Outline each blood parasite and name the species.
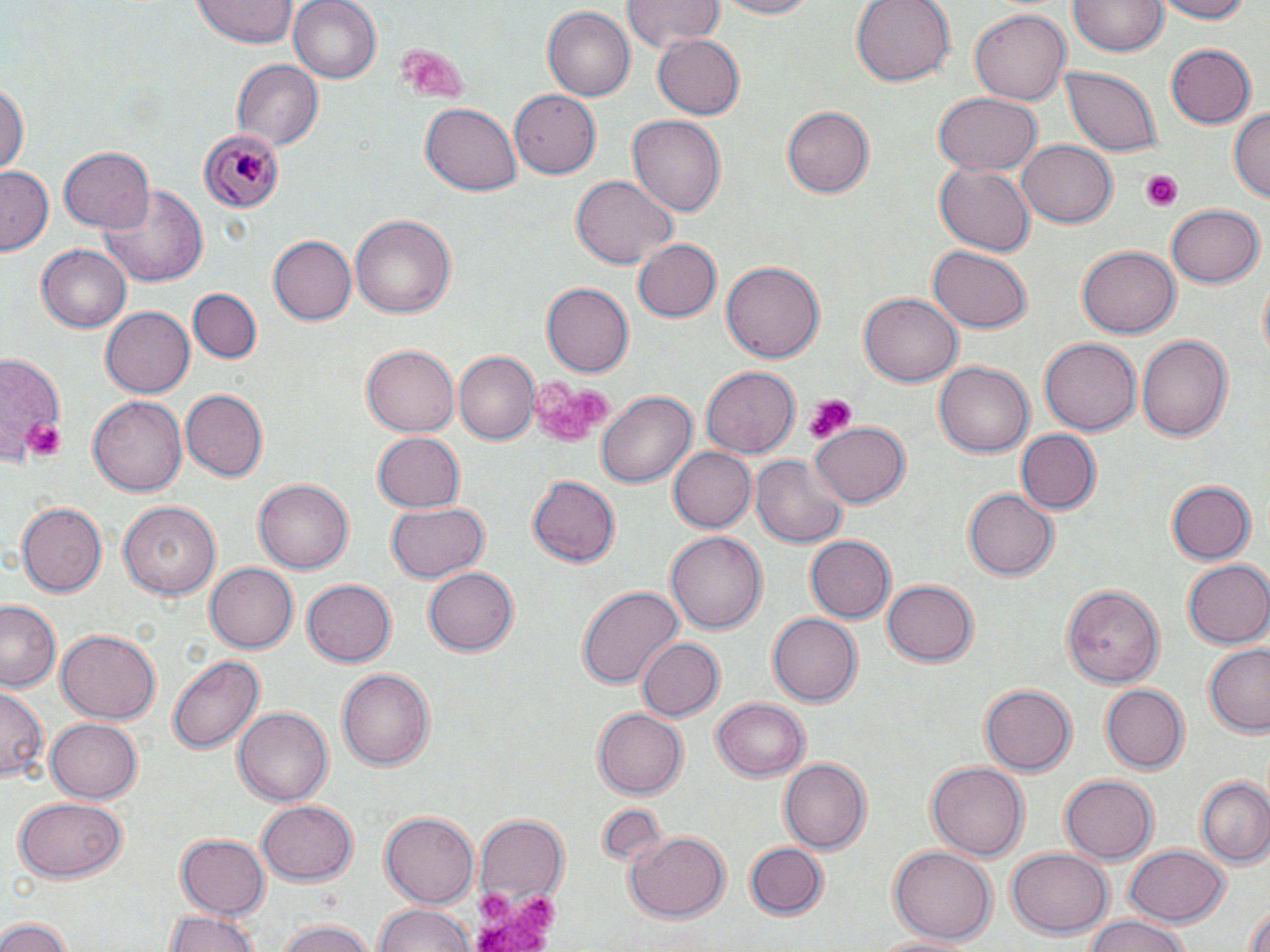

Approximate bounding boxes as (x1,y1)-(x2,y2) corner pairs in pixels.
Plasmodium malariae-infected red blood cells: (199,130)-(286,212).
No Plasmodium falciparum, Plasmodium ovale, Plasmodium vivax, Babesia divergens, or Trypanosoma brucei observed.

slide_level_diagnosis: Plasmodium malariae
field_of_view: one of a larger specimen
preparation: thin blood film
image_size: 1270×952 pixels
uninfected_red_blood_cell_locations: 'approximate bounding boxes as (x1,y1)-(x2,y2) corner pairs in pixels: (195,0)-(298,46), (289,0)-(384,84), (621,0)-(723,53), (704,0)-(820,18), (851,0)-(955,86), (1151,0)-(1254,23), (1071,1)-(1166,57), (544,6)-(635,102), (970,8)-(1071,107), (653,35)-(744,118), (1165,43)-(1255,128), (232,59)-(323,153), (1060,67)-(1163,158), (0,80)-(27,178), (509,89)-(600,177), (932,94)-(1041,178), (420,103)-(520,196), (784,106)-(877,197), (1230,107)-(1270,206), (627,114)-(725,219), (1019,138)-(1116,227), (58,146)-(155,234), (935,164)-(1035,256), (1,166)-(55,256), (569,175)-(679,269), (96,181)-(211,288), (1166,203)-(1262,288), (350,214)-(456,320), (267,234)-(356,325), (630,238)-(720,323), (1079,244)-(1181,337), (928,245)-(1031,331), (38,246)-(131,331), (721,261)-(823,365), (541,282)-(634,377), (190,289)-(260,364), (862,291)-(960,385), (103,305)-(195,399), (1135,332)-(1232,445), (1039,337)-(1140,436), (362,344)-(461,437), (455,350)-(540,444), (0,353)-(78,467), (934,361)-(1034,458), (701,367)-(801,457), (183,388)-(270,481), (595,390)-(695,490), (89,397)-(186,497), (811,419)-(911,507), (1013,429)-(1100,514), (371,431)-(465,513), (667,448)-(755,532), (749,454)-(847,549), (252,477)-(354,574), (527,477)-(620,567), (1166,480)-(1256,565), (963,488)-(1056,580), (14,501)-(106,597), (118,502)-(218,601), (385,502)-(489,583), (666,529)-(768,634), (804,534)-(895,624), (1184,560)-(1270,648), (203,562)-(298,655), (424,568)-(518,657), (302,578)-(399,666), (883,580)-(978,666), (1062,582)-(1164,688), (577,584)-(681,690), (2,600)-(62,693), (769,613)-(861,706), (55,629)-(160,725), (635,638)-(723,723), (1202,645)-(1270,737), (168,654)-(263,755), (337,668)-(436,770), (1100,683)-(1190,775), (979,684)-(1076,776), (0,688)-(46,783), (711,698)-(810,782), (593,707)-(687,798), (233,708)-(332,806), (45,718)-(143,804), (778,757)-(871,854), (927,759)-(1026,857), (1195,774)-(1270,869), (1059,775)-(1158,864), (14,796)-(127,883), (259,797)-(357,884), (599,802)-(666,867), (380,813)-(479,906), (472,814)-(566,918), (628,829)-(729,924), (176,834)-(270,915), (745,841)-(829,918), (1122,844)-(1229,928), (888,847)-(995,943), (1006,849)-(1113,940), (376,903)-(472,952), (1243,904)-(1270,952), (164,908)-(264,952), (1078,917)-(1198,952), (0,918)-(75,952), (275,919)-(379,952), (869,931)-(981,951)'
stain: May-Grünwald-Giemsa
magnification: 1000x
platelet_locations: 'approximate bounding boxes as (x1,y1)-(x2,y2) corner pairs in pixels: (398,44)-(468,96), (1139,171)-(1184,210), (526,376)-(609,439), (801,396)-(856,442), (20,417)-(63,458), (472,878)-(560,950)'
modality: optical microscopy